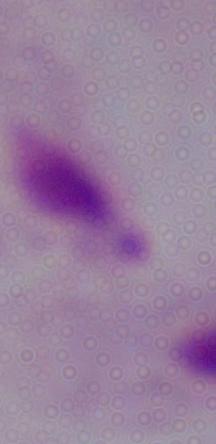

identification: trichomonad
magnification: 1000x
modality: micrograph